State which parasite is depicted.
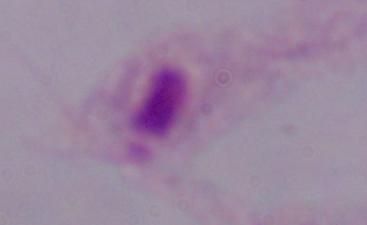
This is a trichomonad.

Summary:
  - Modality: micrograph
  - Magnification: 1000x